Name the parasite shown.
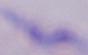

This is a trypanosome.

Captured at 1000x magnification. Photomicrograph.